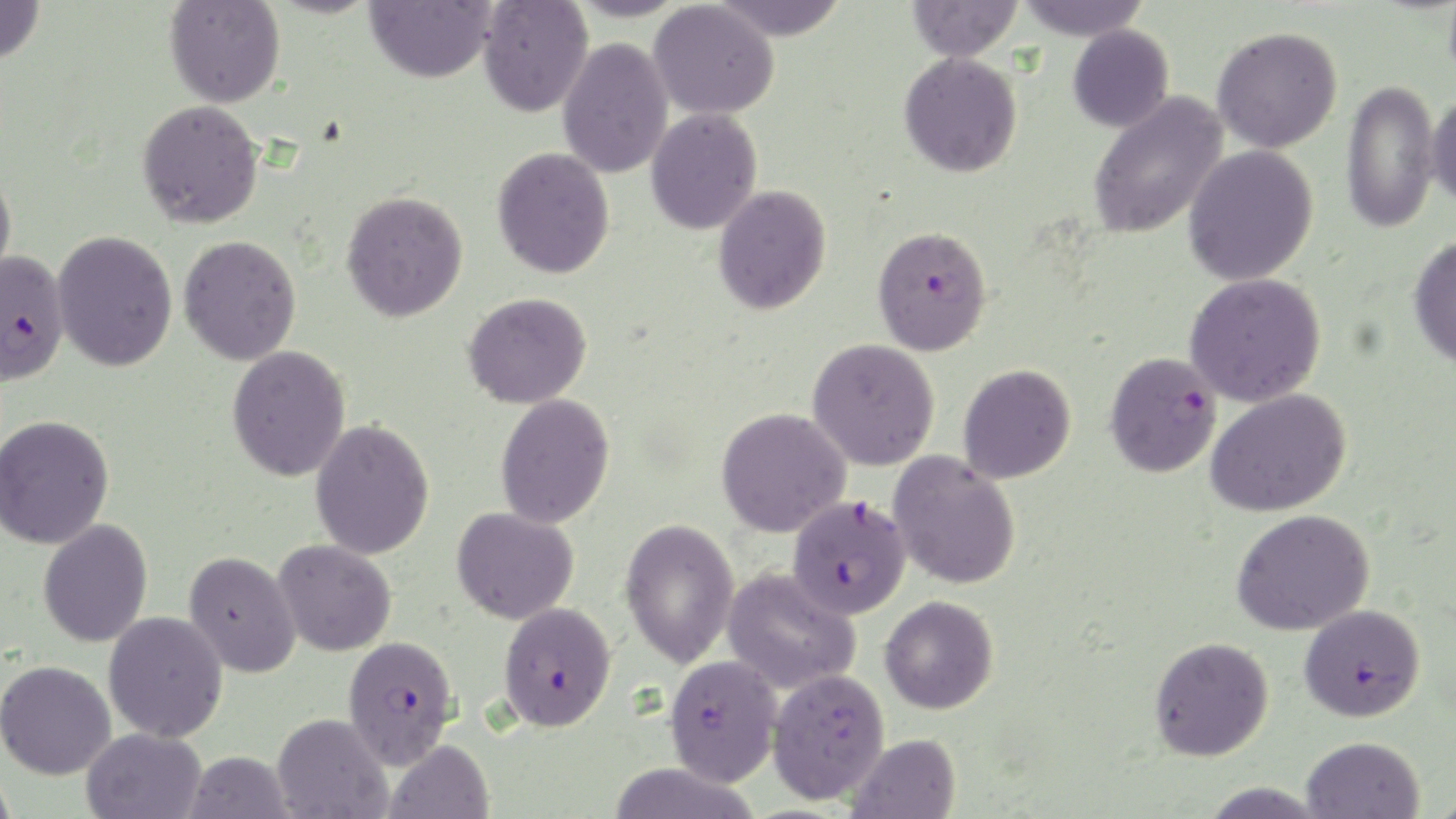
slide-level diagnosis = Plasmodium falciparum
stain = May-Grünwald-Giemsa
preparation = thin blood film
magnification = 1000x
image size = 1456×819 pixels
Plasmodium falciparum-infected red blood cell locations = approximate bounding boxes as [x1, y1, x2, y2] in pixels: [872, 225, 991, 355], [0, 250, 69, 385], [1105, 351, 1223, 478], [787, 495, 911, 619], [498, 602, 617, 732], [1299, 603, 1425, 722], [343, 634, 459, 771], [664, 654, 783, 786]
modality = optical microscopy
field of view = one of a larger specimen
uninfected red blood cell locations = approximate bounding boxes as [x1, y1, x2, y2] in pixels: [0, 0, 45, 66], [365, 0, 495, 83], [566, 0, 689, 23], [707, 0, 850, 40], [906, 0, 1023, 62], [1014, 0, 1153, 40], [164, 1, 285, 108], [478, 1, 593, 117], [649, 2, 779, 120], [1067, 24, 1174, 132], [1212, 26, 1343, 153], [557, 37, 674, 179], [899, 52, 1023, 177], [1341, 78, 1441, 234], [1426, 91, 1456, 211], [1087, 92, 1229, 241], [137, 99, 264, 228], [645, 107, 763, 235], [1183, 145, 1319, 286], [492, 147, 615, 279], [0, 167, 17, 290], [713, 185, 832, 315], [341, 190, 468, 322], [52, 229, 178, 372], [1407, 234, 1456, 369], [179, 235, 302, 366], [1184, 273, 1327, 407], [463, 292, 592, 408], [807, 338, 940, 470], [226, 345, 351, 482], [958, 363, 1077, 484], [1207, 387, 1352, 516], [495, 393, 615, 529], [716, 407, 851, 537], [0, 415, 115, 549], [310, 418, 435, 560], [888, 450, 1021, 590], [452, 506, 580, 625], [1232, 509, 1374, 635], [620, 517, 740, 669], [38, 518, 153, 647], [272, 539, 397, 657], [183, 551, 301, 678], [722, 567, 861, 696], [880, 594, 999, 714], [103, 611, 228, 742], [1149, 636, 1274, 761], [0, 660, 116, 780], [767, 667, 890, 804], [272, 713, 392, 819], [81, 727, 206, 819], [847, 733, 961, 819], [1301, 736, 1425, 819], [385, 739, 494, 819], [184, 751, 294, 818], [606, 762, 762, 819], [0, 765, 17, 819], [1197, 781, 1330, 818]